Identify the parasite.
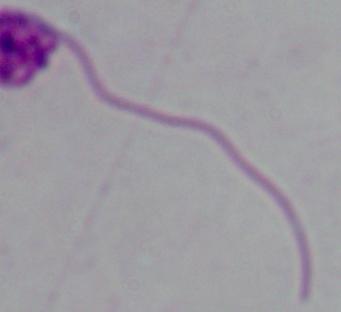
This is Leishmania.

Summary:
  - Modality: micrograph
  - Magnification: 1000x